Classify this cell by malaria status.
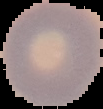
Uninfected.

Summary:
  - Image size: 103×109 pixels
  - Preparation: thin blood smear
  - Image type: segmented cell region on a black background